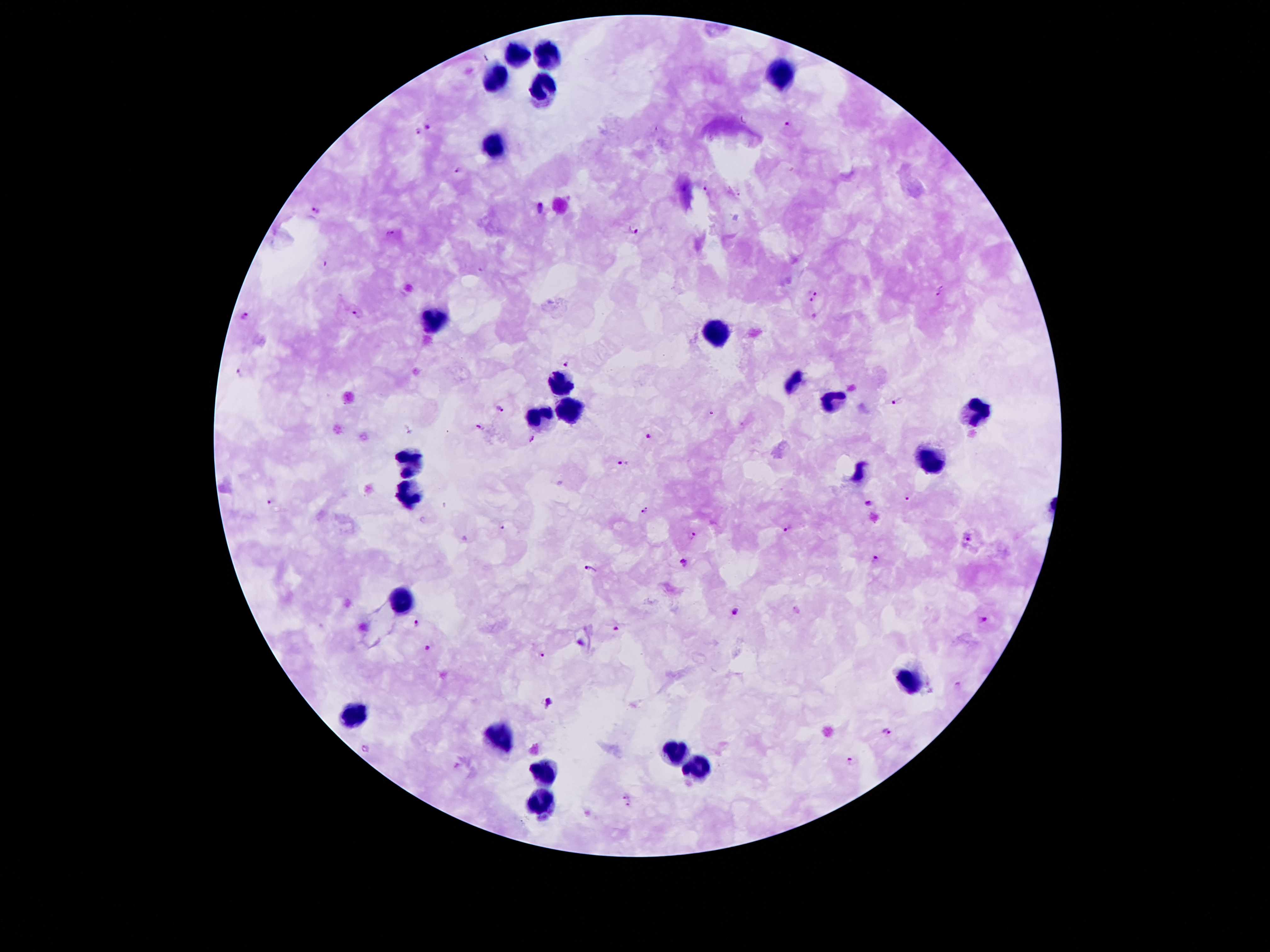 Approximate centers as (x, y) in pixels. Leukocyte locations: (515, 53), (550, 58), (494, 72), (780, 72), (539, 93), (490, 144), (436, 322), (716, 330), (557, 379), (795, 383), (830, 402), (572, 409), (970, 412), (537, 413), (408, 459), (927, 460), (410, 494), (399, 603), (912, 681), (352, 715), (498, 739), (675, 752), (697, 765), (541, 774), (541, 800). Malaria parasite locations: (788, 124), (430, 126), (418, 132), (460, 169), (705, 190), (541, 209), (316, 210), (635, 229), (390, 234), (939, 293), (816, 294), (359, 314), (245, 315), (568, 362), (238, 370), (897, 401), (501, 408), (477, 426), (649, 434), (532, 438), (621, 461), (908, 497), (268, 502), (870, 502), (644, 510), (503, 528), (788, 530), (695, 537), (969, 540), (875, 558), (684, 559), (590, 568), (737, 610), (984, 619), (418, 626), (616, 627), (583, 640), (427, 648), (543, 656), (551, 701), (888, 731), (365, 750), (850, 761), (628, 801). Giemsa stain. 100x magnification. Thick blood film. Photographed through the microscope eyepiece with a smartphone camera. Image is 1270×952 pixels. Patient malaria status: infected with Plasmodium falciparum. Single field of view.